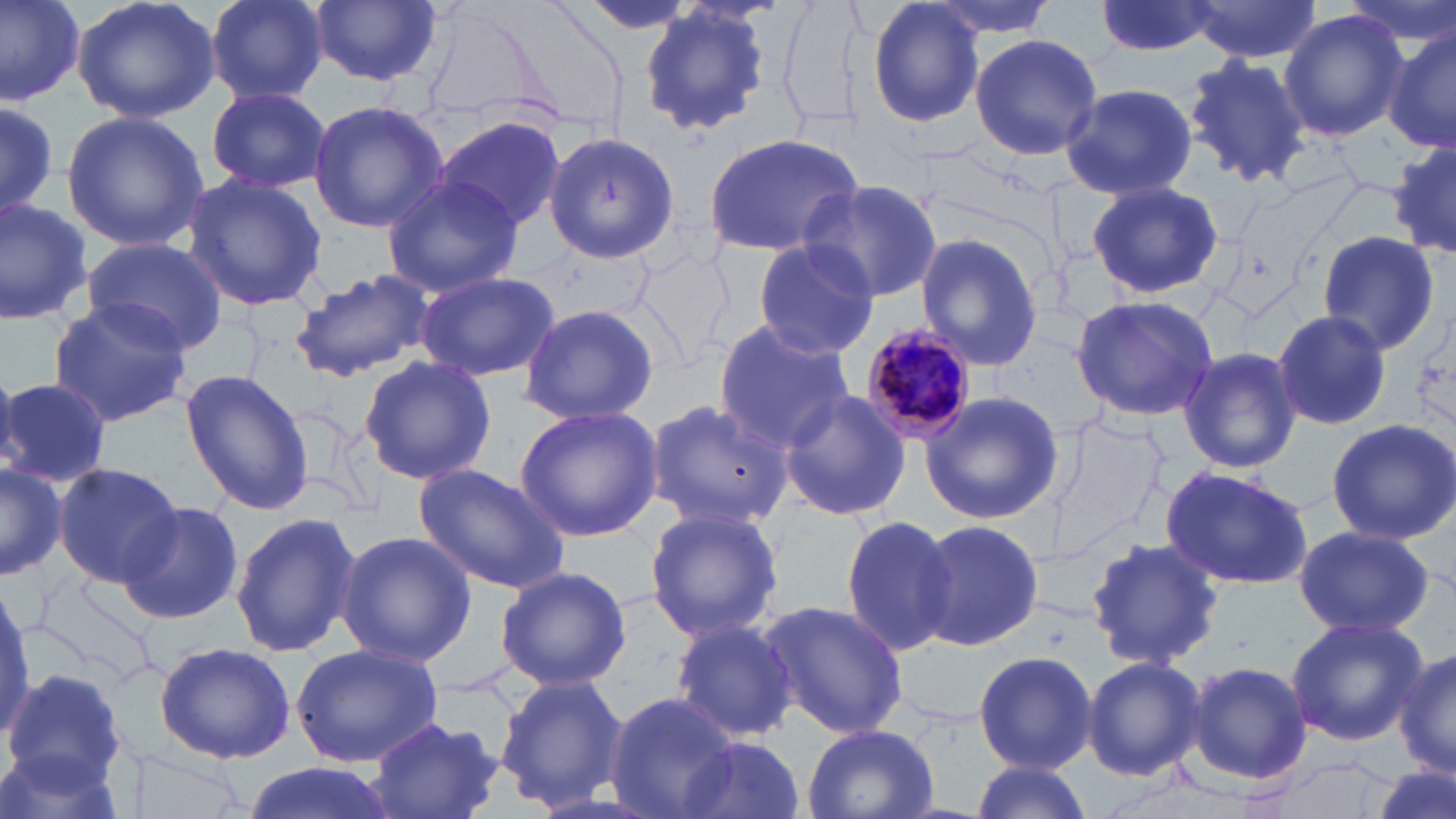
Summary:
  - Coordinate format: approximate bounding boxes as named x1/y1/x2/y2 corners in pixels
  - Plasmodium malariae-infected red blood cell locations: (x1=857, y1=324, x2=977, y2=451)
  - Uninfected red blood cell locations: (x1=0, y1=0, x2=85, y2=105), (x1=72, y1=0, x2=223, y2=124), (x1=203, y1=0, x2=330, y2=103), (x1=309, y1=0, x2=444, y2=86), (x1=924, y1=0, x2=1062, y2=38), (x1=1094, y1=0, x2=1221, y2=57), (x1=1342, y1=0, x2=1456, y2=45), (x1=866, y1=1, x2=985, y2=129), (x1=1186, y1=1, x2=1321, y2=62), (x1=638, y1=5, x2=771, y2=139), (x1=1278, y1=10, x2=1406, y2=140), (x1=1383, y1=27, x2=1456, y2=157), (x1=969, y1=31, x2=1103, y2=161), (x1=1181, y1=52, x2=1310, y2=189), (x1=1060, y1=82, x2=1199, y2=202), (x1=205, y1=86, x2=331, y2=194), (x1=0, y1=98, x2=57, y2=221), (x1=307, y1=100, x2=448, y2=233), (x1=60, y1=110, x2=209, y2=252), (x1=434, y1=117, x2=568, y2=235), (x1=701, y1=131, x2=867, y2=257), (x1=547, y1=132, x2=679, y2=263), (x1=1388, y1=140, x2=1456, y2=262), (x1=181, y1=173, x2=327, y2=312), (x1=379, y1=176, x2=521, y2=299), (x1=802, y1=179, x2=945, y2=302), (x1=1085, y1=179, x2=1226, y2=303), (x1=0, y1=195, x2=92, y2=324), (x1=1314, y1=230, x2=1441, y2=356), (x1=913, y1=233, x2=1046, y2=371), (x1=80, y1=235, x2=227, y2=356), (x1=751, y1=239, x2=883, y2=357), (x1=289, y1=266, x2=438, y2=383), (x1=413, y1=270, x2=560, y2=382), (x1=1069, y1=295, x2=1218, y2=423), (x1=46, y1=299, x2=193, y2=426), (x1=517, y1=302, x2=659, y2=426), (x1=1272, y1=310, x2=1393, y2=429), (x1=712, y1=319, x2=853, y2=455), (x1=1178, y1=347, x2=1301, y2=474), (x1=357, y1=354, x2=497, y2=486), (x1=180, y1=369, x2=315, y2=515), (x1=0, y1=376, x2=114, y2=488), (x1=778, y1=389, x2=912, y2=521), (x1=919, y1=389, x2=1066, y2=525), (x1=647, y1=397, x2=791, y2=532), (x1=514, y1=402, x2=666, y2=542), (x1=1324, y1=419, x2=1456, y2=542), (x1=0, y1=460, x2=65, y2=582), (x1=54, y1=462, x2=186, y2=587), (x1=410, y1=463, x2=572, y2=595), (x1=1160, y1=464, x2=1315, y2=590), (x1=120, y1=499, x2=246, y2=625), (x1=644, y1=503, x2=783, y2=645), (x1=230, y1=512, x2=361, y2=660), (x1=840, y1=514, x2=957, y2=656), (x1=914, y1=519, x2=1045, y2=651), (x1=1293, y1=525, x2=1434, y2=639), (x1=335, y1=531, x2=477, y2=667), (x1=1083, y1=537, x2=1225, y2=669), (x1=495, y1=565, x2=631, y2=692), (x1=759, y1=599, x2=909, y2=742), (x1=1285, y1=616, x2=1427, y2=745), (x1=668, y1=617, x2=800, y2=743), (x1=154, y1=641, x2=297, y2=763), (x1=292, y1=643, x2=446, y2=766), (x1=972, y1=650, x2=1097, y2=772), (x1=1394, y1=650, x2=1456, y2=781), (x1=1082, y1=655, x2=1206, y2=780), (x1=1185, y1=660, x2=1313, y2=787), (x1=5, y1=667, x2=128, y2=790), (x1=493, y1=676, x2=628, y2=811), (x1=605, y1=692, x2=741, y2=819), (x1=365, y1=716, x2=504, y2=819), (x1=802, y1=723, x2=940, y2=819), (x1=676, y1=734, x2=808, y2=819), (x1=0, y1=745, x2=127, y2=819), (x1=118, y1=745, x2=250, y2=817), (x1=1267, y1=756, x2=1391, y2=818), (x1=967, y1=760, x2=1092, y2=819), (x1=240, y1=761, x2=396, y2=819), (x1=1370, y1=763, x2=1454, y2=819)
  - Slide-level diagnosis: Plasmodium malariae
  - Stain: May-Grünwald-Giemsa
  - Field of view: one of a larger specimen
  - Modality: light microscopy
  - Image size: 1456×819 pixels
  - Preparation: thin blood film
  - Magnification: 1000x